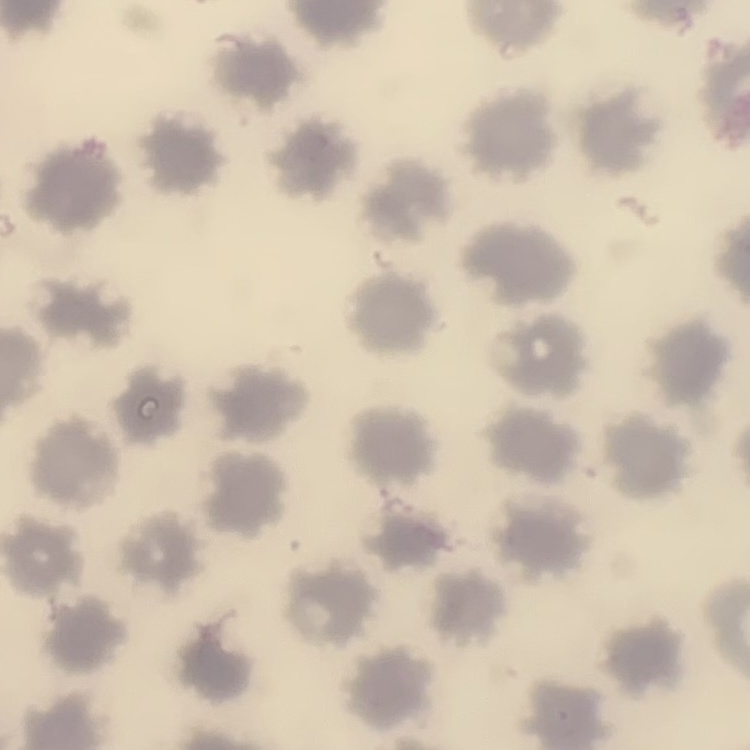
erythrocyte_morphology: no rouleaux formation
image_type: one tile cut from a larger photomicrograph
stain: Field's or Giemsa
preparation: thin peripheral smear